Locate every Plasmodium parasite.
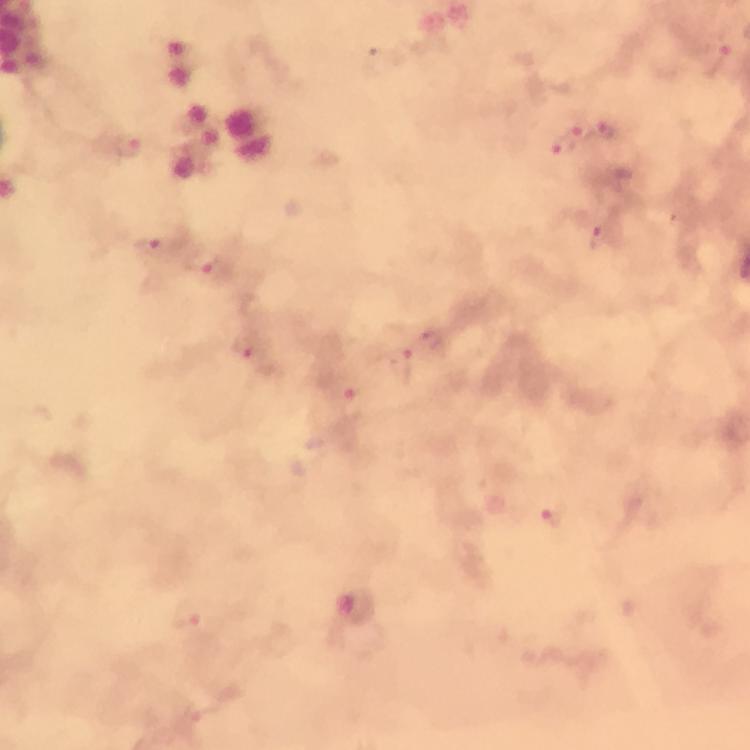
Approximate centers as [x, y] in pixels.
Plasmodium parasites: [715, 61], [610, 132], [583, 134], [126, 146], [563, 149], [601, 238], [153, 248], [202, 262], [432, 341], [247, 350], [402, 368], [355, 406], [554, 518], [185, 614].

Summary:
  - Stain: Giemsa
  - Magnification: 100x
  - Immersion oil: applied
  - Image size: 750×750 pixels
  - Preparation: thick blood film
  - Context: from a malaria diagnostic workup
  - Capture: smartphone mounted on the microscope
  - Cropped from: one field of view